Identify the parasite.
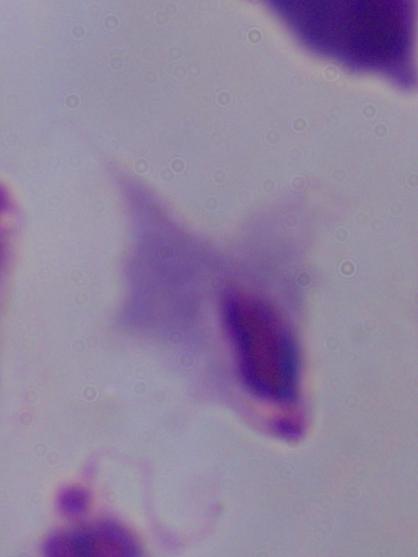

This is a trichomonad.

Summary:
  - Modality: micrograph
  - Magnification: 1000x